Assess the morphology of the erythrocytes.
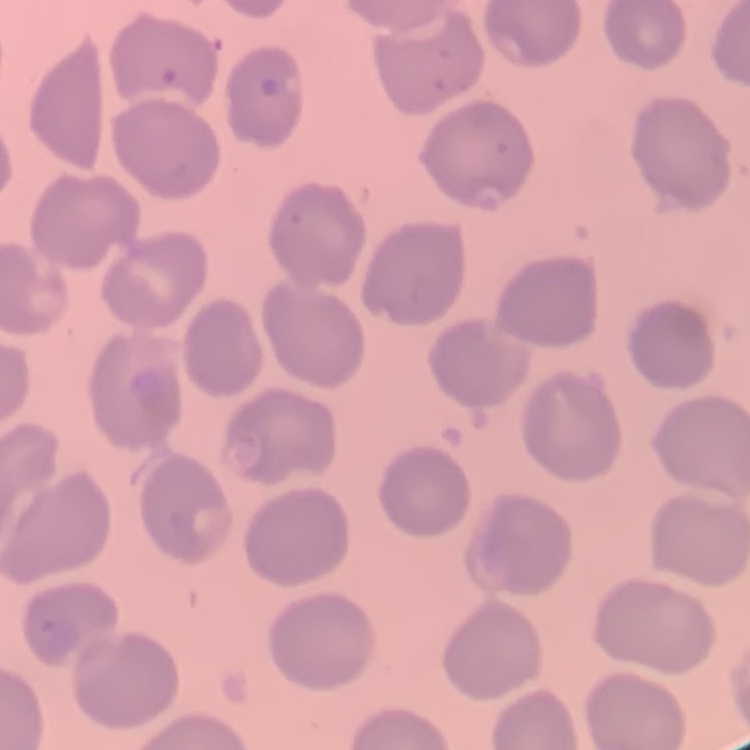

No rouleaux formation.

Summary:
  - Image type: square crop of a larger photomicrograph
  - Preparation: thin blood smear
  - Stain: Field's or Giemsa